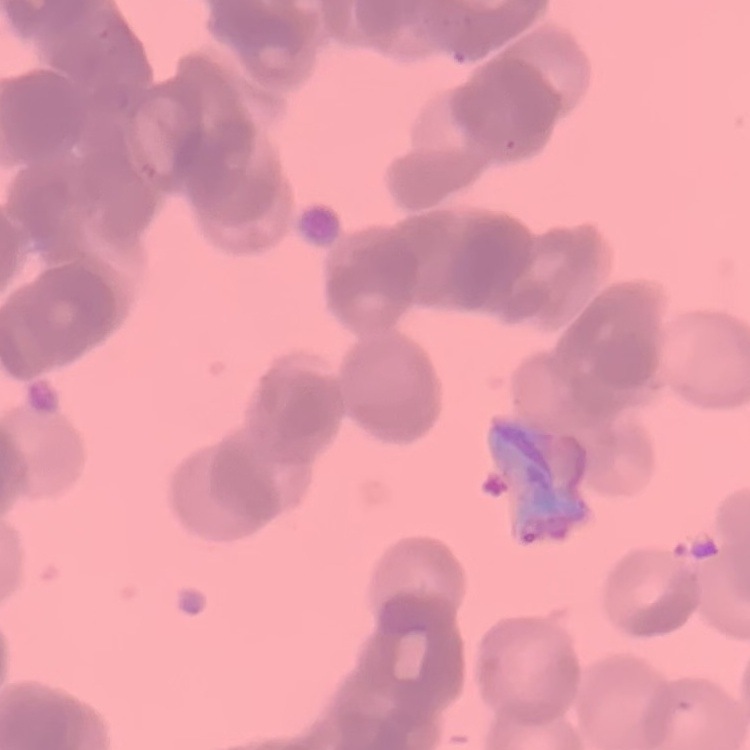 The red blood cells exhibit rouleaux formation. One tile cut from a larger photomicrograph. Thin blood film. Field's or Giemsa stain.